State the blood parasite species.
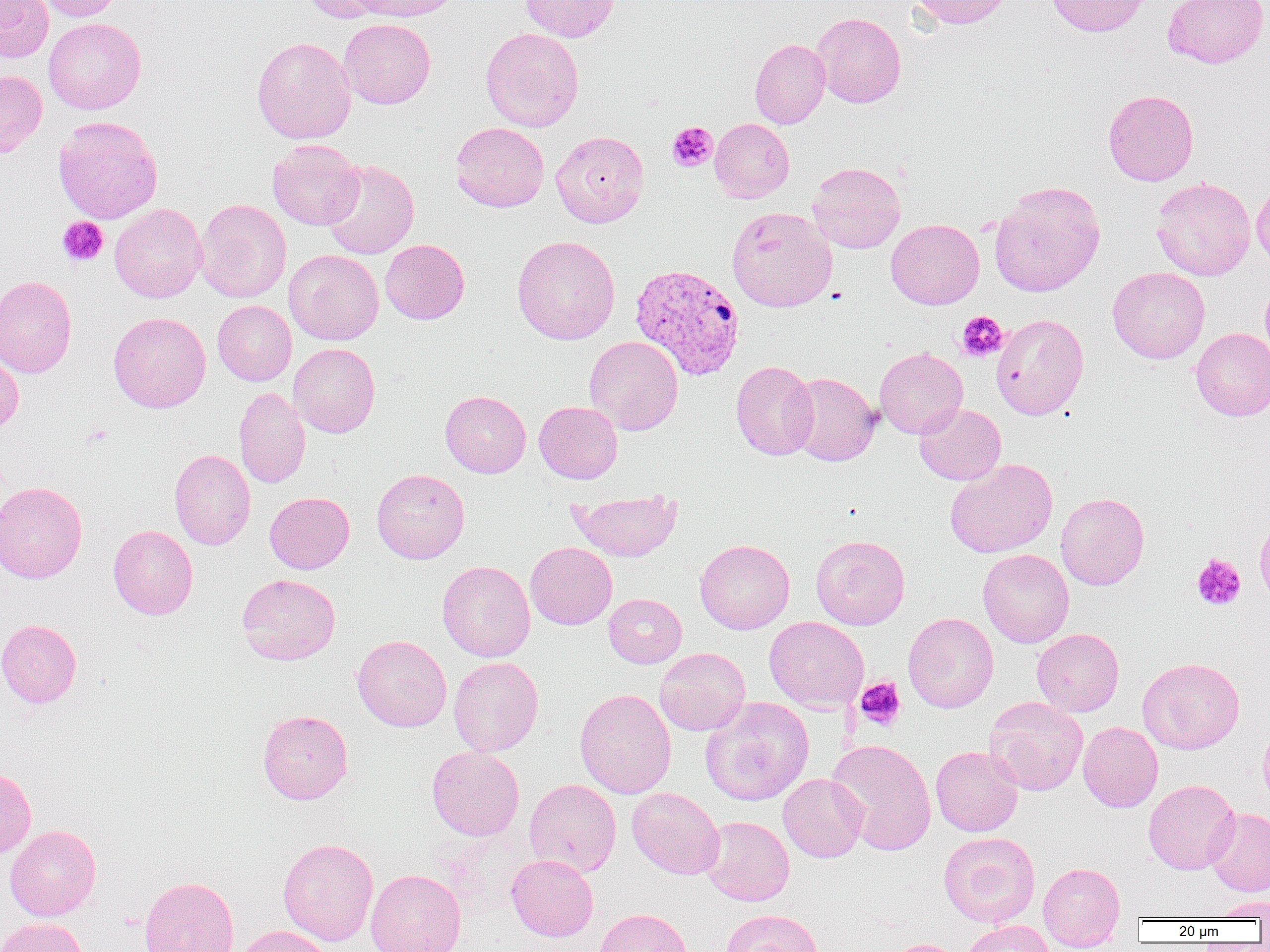

Plasmodium vivax.

Approximate bounding boxes as (x1, y1, x2, y2) in pixels. Platelet locations: (667, 121, 717, 172), (57, 216, 108, 266), (956, 311, 1008, 362), (1191, 553, 1246, 611), (855, 677, 906, 730). Uninfected red blood cell locations: (0, 0, 53, 62), (35, 0, 121, 21), (298, 0, 389, 23), (352, 0, 464, 22), (520, 0, 620, 41), (910, 0, 1016, 28), (1045, 0, 1149, 37), (1163, 0, 1269, 68), (811, 12, 906, 108), (43, 18, 146, 114), (338, 18, 435, 109), (481, 28, 584, 131), (252, 36, 356, 144), (750, 38, 831, 129), (0, 70, 47, 157), (1103, 89, 1199, 186), (52, 116, 163, 224), (710, 118, 794, 202), (450, 122, 549, 212), (550, 130, 649, 227), (267, 139, 365, 230), (321, 159, 419, 259), (808, 162, 905, 253), (1151, 177, 1255, 281), (1251, 178, 1270, 270), (989, 181, 1105, 297), (195, 199, 291, 303), (109, 203, 207, 302), (726, 206, 837, 312), (886, 218, 984, 309), (512, 235, 620, 344), (380, 239, 469, 324), (284, 249, 384, 345), (1108, 267, 1210, 364), (0, 275, 77, 378), (1260, 279, 1270, 362), (213, 300, 296, 385), (108, 311, 211, 413), (991, 313, 1089, 419), (1191, 328, 1270, 421), (584, 335, 683, 435), (289, 343, 380, 437), (874, 347, 968, 438), (0, 350, 24, 433), (731, 361, 818, 461), (786, 372, 881, 466), (234, 386, 311, 488), (440, 390, 531, 477), (534, 401, 623, 483), (914, 403, 1006, 485), (169, 449, 256, 550), (945, 458, 1058, 558), (372, 468, 469, 563), (0, 480, 88, 584), (568, 489, 682, 561), (265, 492, 355, 574), (1056, 492, 1149, 590), (1254, 516, 1270, 607), (108, 525, 197, 620), (811, 535, 910, 630), (695, 539, 795, 634), (525, 542, 617, 629), (978, 548, 1074, 648), (437, 560, 535, 662), (237, 573, 340, 664), (604, 594, 687, 668), (903, 612, 998, 713), (764, 616, 869, 711), (0, 619, 82, 708), (1032, 628, 1124, 716), (352, 634, 451, 732), (655, 648, 751, 735), (449, 656, 544, 756), (1138, 657, 1245, 754), (575, 688, 676, 799), (700, 696, 814, 806), (984, 697, 1088, 795), (257, 709, 353, 804), (1078, 721, 1163, 812), (1258, 722, 1270, 808), (827, 739, 937, 855), (427, 745, 524, 840), (931, 746, 1023, 836), (0, 766, 37, 858), (778, 773, 868, 862), (524, 778, 621, 877), (1143, 779, 1241, 874), (627, 787, 725, 879), (1205, 807, 1270, 896), (700, 816, 794, 906), (5, 825, 101, 921), (939, 832, 1040, 927), (277, 837, 379, 945), (506, 854, 598, 941), (1038, 861, 1125, 949), (366, 869, 466, 952), (138, 876, 239, 952), (1210, 896, 1270, 920), (593, 907, 692, 952), (720, 908, 822, 952), (0, 917, 88, 952), (961, 920, 1056, 952), (235, 925, 335, 952), (881, 938, 966, 952). Plasmodium vivax-infected red blood cell locations: (630, 262, 745, 380). Thin blood film. One field of a larger specimen. Image is 1270×952 pixels. Optical microscopy. 1000x magnification.